Report the malaria status of this cell.
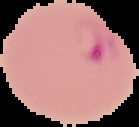

It is parasitized.

Summary:
  - Preparation: thin blood smear
  - Image size: 139×127 pixels
  - Image type: segmented cell region on a black background